Identify the preparation type.
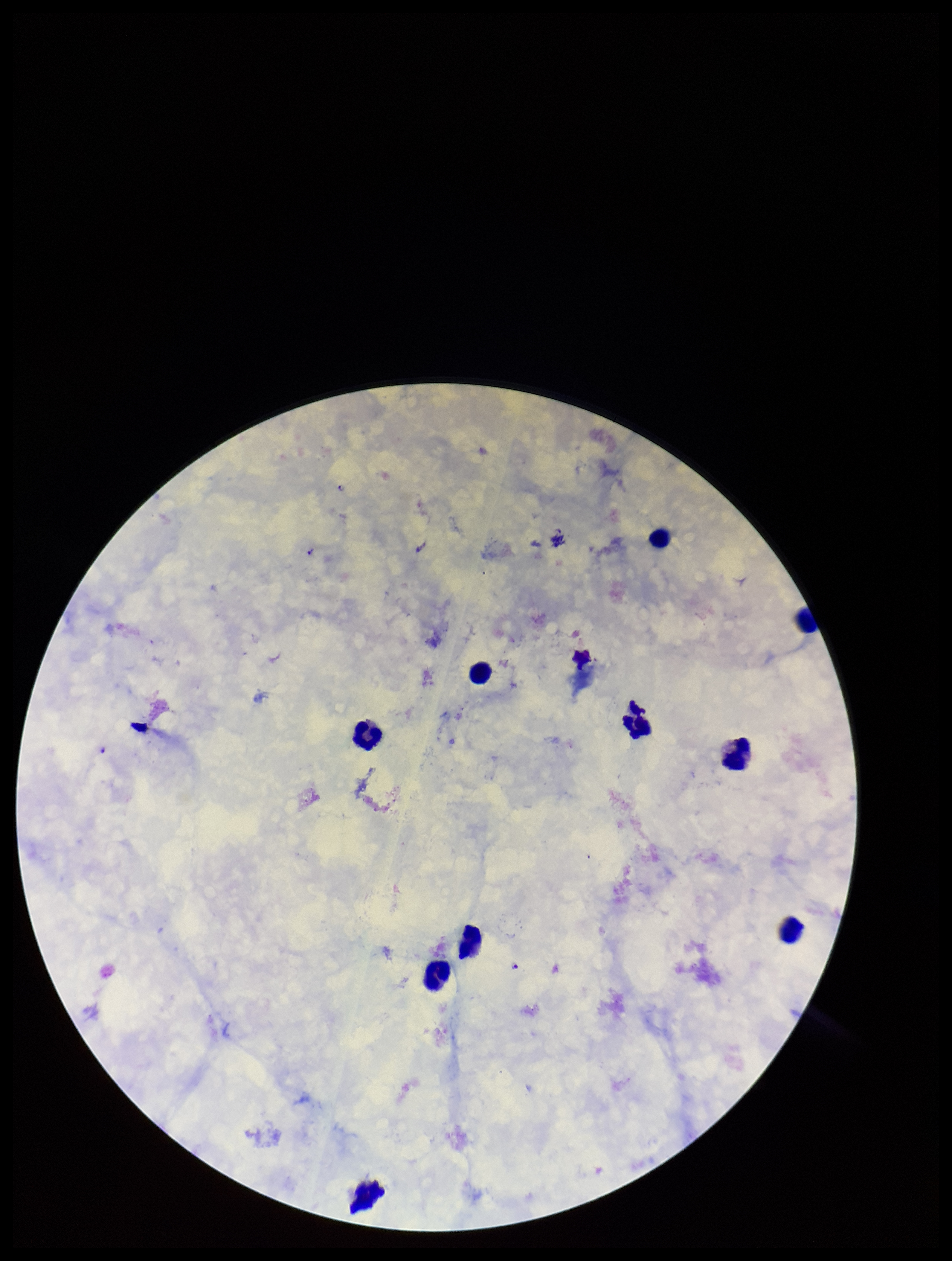
Thick.

parasite count = 2
image size = 952×1261 pixels
field of view = single
capture = smartphone photograph through the microscope eyepiece
species reported for this patient = Plasmodium falciparum
stain = Giemsa
patient malaria status = infected
Plasmodium parasites = identified
leukocyte count = 10